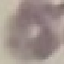

Summary:
  - Result: negative for malaria parasites
  - Image type: cell patch, automatically extracted from a larger field of view and resized to 64 × 64 pixels
  - Capture: smartphone camera at the microscope eyepiece
  - Preparation: thin smear
  - Stain: Giemsa